Report the malaria status of this cell.
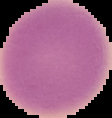

It is uninfected.

Summary:
  - Preparation: thin blood film
  - Image size: 112×118 pixels
  - Image type: cell region segmented out of the field of view; surrounding area masked to black